Name the parasite shown.
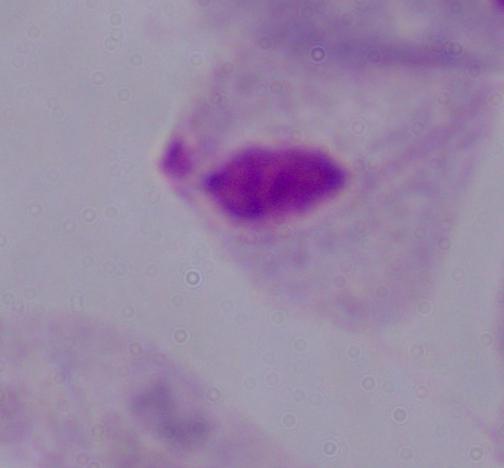

A trichomonad.

{
  "modality": "micrograph",
  "magnification": "1000x"
}